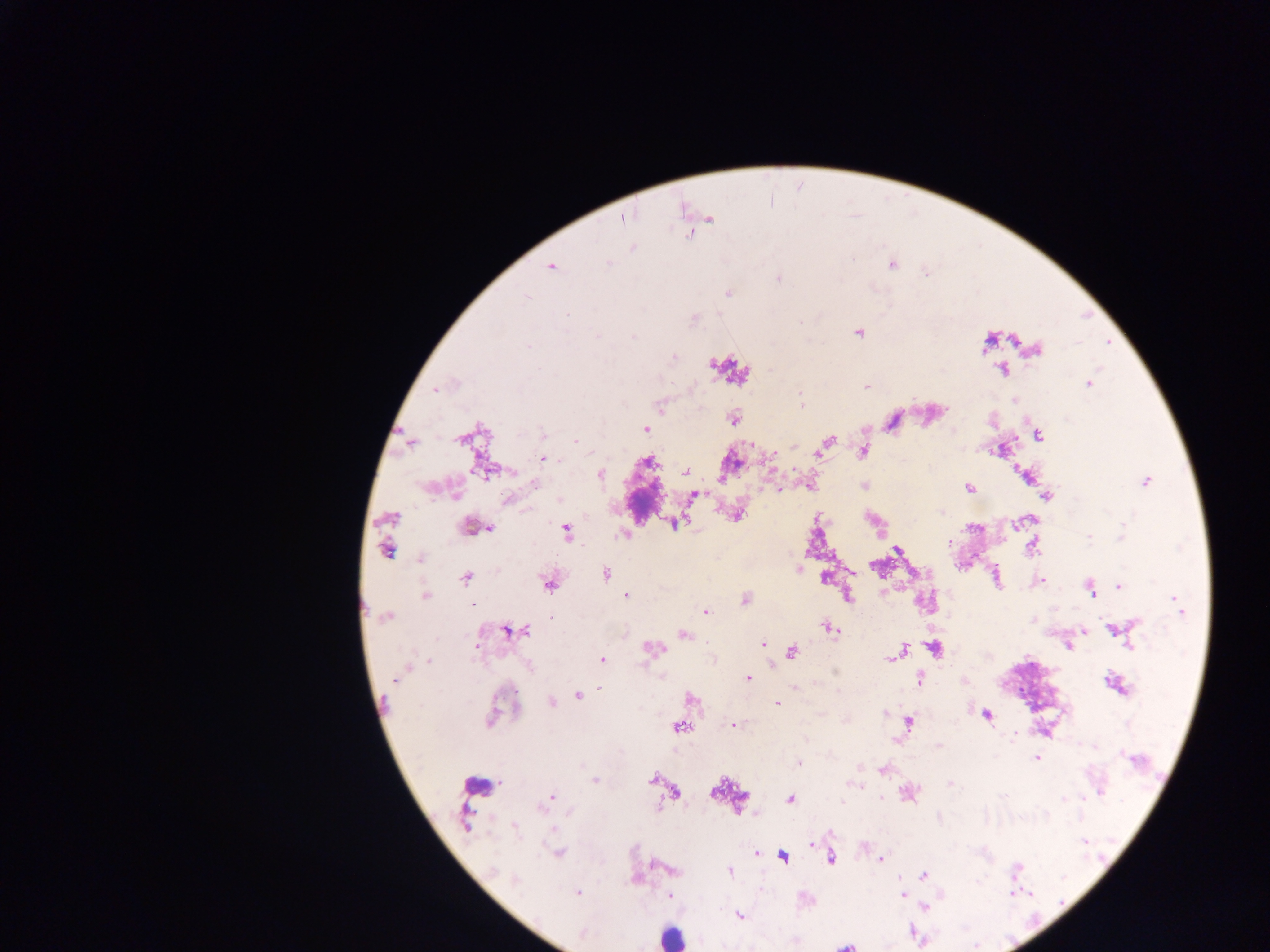
Approximate centers as {x, y} in pixels.
Summary:
  - Malaria parasite locations: {624, 218}, {712, 218}, {689, 235}, {633, 247}, {609, 263}, {892, 264}, {551, 267}, {926, 273}, {778, 278}, {727, 293}, {526, 298}, {567, 315}, {694, 320}, {858, 333}, {596, 335}, {633, 337}, {528, 346}, {1035, 350}, {674, 358}, {1002, 370}, {1089, 383}, {867, 387}, {438, 388}, {801, 400}, {1014, 400}, {660, 407}, {734, 420}, {646, 428}, {542, 434}, {1037, 435}, {576, 441}, {828, 441}, {410, 443}, {821, 452}, {862, 452}, {544, 459}, {647, 462}, {686, 472}, {601, 475}, {1146, 482}, {534, 483}, {863, 486}, {970, 487}, {696, 496}, {1047, 497}, {559, 500}, {508, 501}, {737, 515}, {392, 517}, {674, 523}, {469, 526}, {490, 529}, {567, 532}, {1122, 533}, {622, 536}, {1089, 538}, {949, 541}, {1031, 547}, {387, 550}, {898, 550}, {420, 559}, {798, 568}, {606, 574}, {466, 578}, {1041, 580}, {548, 584}, {1119, 587}, {1091, 590}, {425, 595}, {626, 596}, {848, 596}, {745, 599}, {473, 604}, {1177, 604}, {706, 611}, {385, 618}, {552, 618}, {830, 628}, {1113, 629}, {1083, 630}, {508, 631}, {525, 631}, {684, 636}, {763, 643}, {1068, 646}, {1129, 646}, {903, 647}, {934, 648}, {653, 649}, {792, 652}, {898, 652}, {891, 657}, {602, 659}, {429, 660}, {748, 678}, {395, 679}, {920, 679}, {1116, 684}, {601, 688}, {578, 697}, {692, 700}, {551, 702}, {777, 703}, {884, 713}, {987, 715}, {491, 719}, {909, 722}, {734, 725}, {679, 727}, {895, 741}, {1094, 746}, {1036, 758}, {1132, 759}, {800, 763}, {883, 770}, {652, 778}, {594, 779}, {950, 784}, {676, 792}, {1101, 792}, {909, 794}, {881, 797}, {551, 798}, {1063, 799}, {790, 800}, {842, 801}, {514, 827}, {1083, 841}, {558, 852}, {757, 854}, {783, 857}, {830, 858}, {881, 859}, {1017, 868}, {729, 872}, {924, 875}, {515, 879}, {577, 893}, {902, 894}, {669, 895}, {925, 906}, {739, 916}, {582, 935}, {845, 945}
  - Leukocyte locations: {671, 936}
  - Country: Ghana
  - Image size: 1270×952 pixels
  - Preparation: thick blood film
  - Field of view: single
  - Capture: mobile-phone photograph through a microscope